Give the position of every Plasmodium falciparum parasite, noting its life-cycle stage.
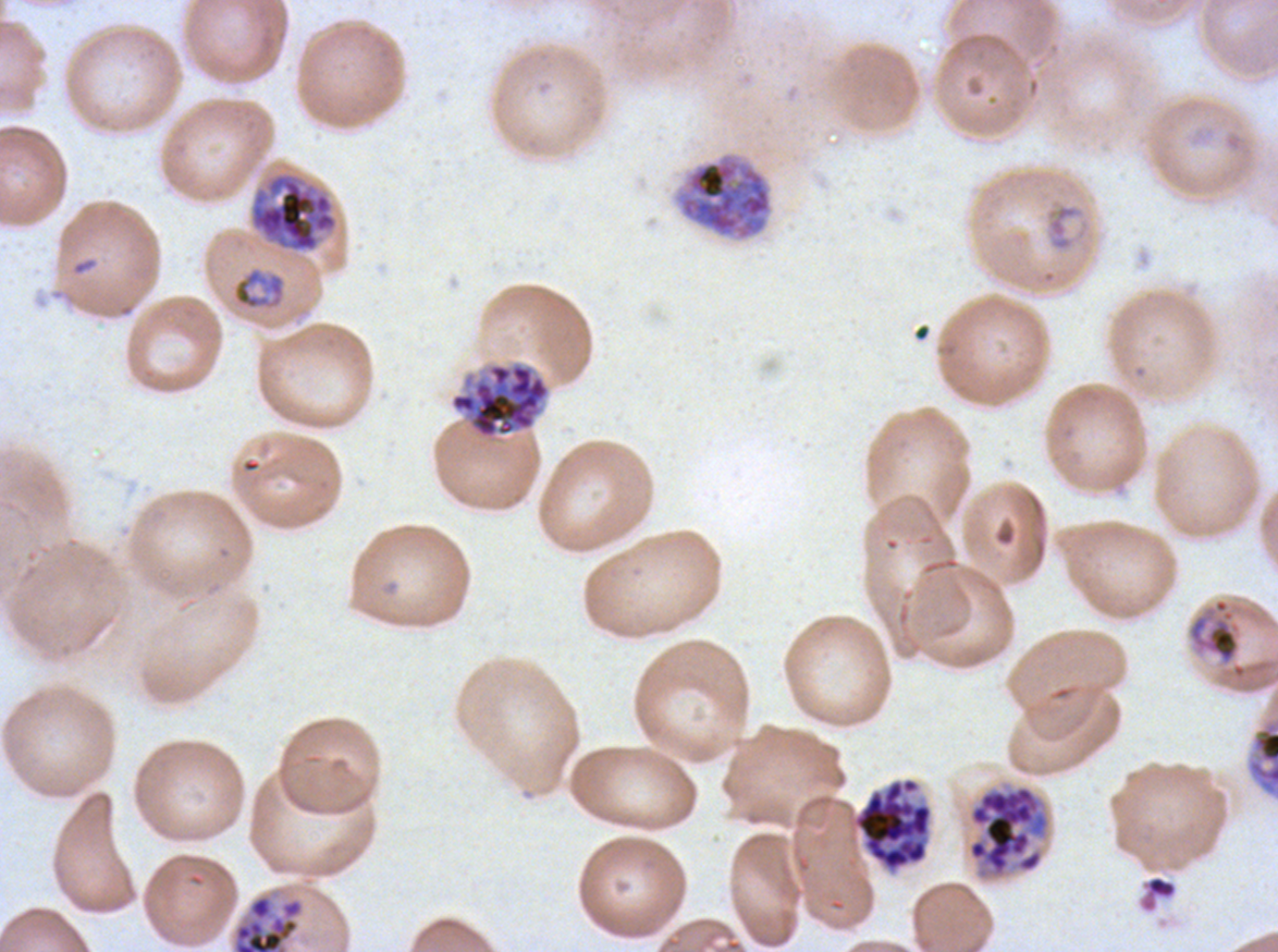

Approximate bounding rectangles given as corner coordinates in pixels from the top-left.
Rings: (x1=1043, y1=198, x2=1090, y2=253).
Mid trophozoites: (x1=232, y1=267, x2=286, y2=311), (x1=1187, y1=597, x2=1241, y2=666).
Late trophozoites: (x1=1246, y1=716, x2=1277, y2=798).
Early schizonts: (x1=673, y1=152, x2=773, y2=241), (x1=250, y1=172, x2=338, y2=252).
Late schizonts: (x1=966, y1=784, x2=1051, y2=880), (x1=230, y1=892, x2=305, y2=951).
Segmenters: (x1=449, y1=360, x2=551, y2=441), (x1=847, y1=776, x2=934, y2=876).
No late-ring/early-trophozoite forms or gametocytes observed.

Debris locations: (x1=1139, y1=874, x2=1178, y2=912). Image is 1278×952 pixels. A sub-image separated from a larger composite. Life-cycle stages observed: ring, mid trophozoite, late trophozoite, early schizont, late schizont, segmenter. Thin blood smear. Giemsa stain. Plasmodium falciparum from a patient in The Gambia, cultured ex vivo for 24 to 48 hours.